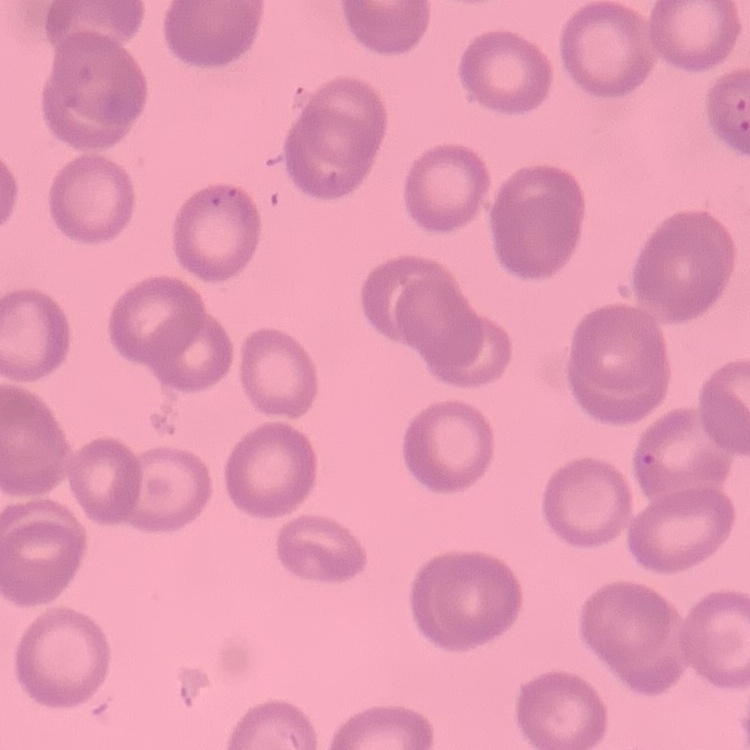 The red blood cells show no rouleaux formation. Thin blood film. One tile cut from a larger photomicrograph. Field's or Giemsa stain.